Locate every P. falciparum parasite and identify its life-cycle stage.
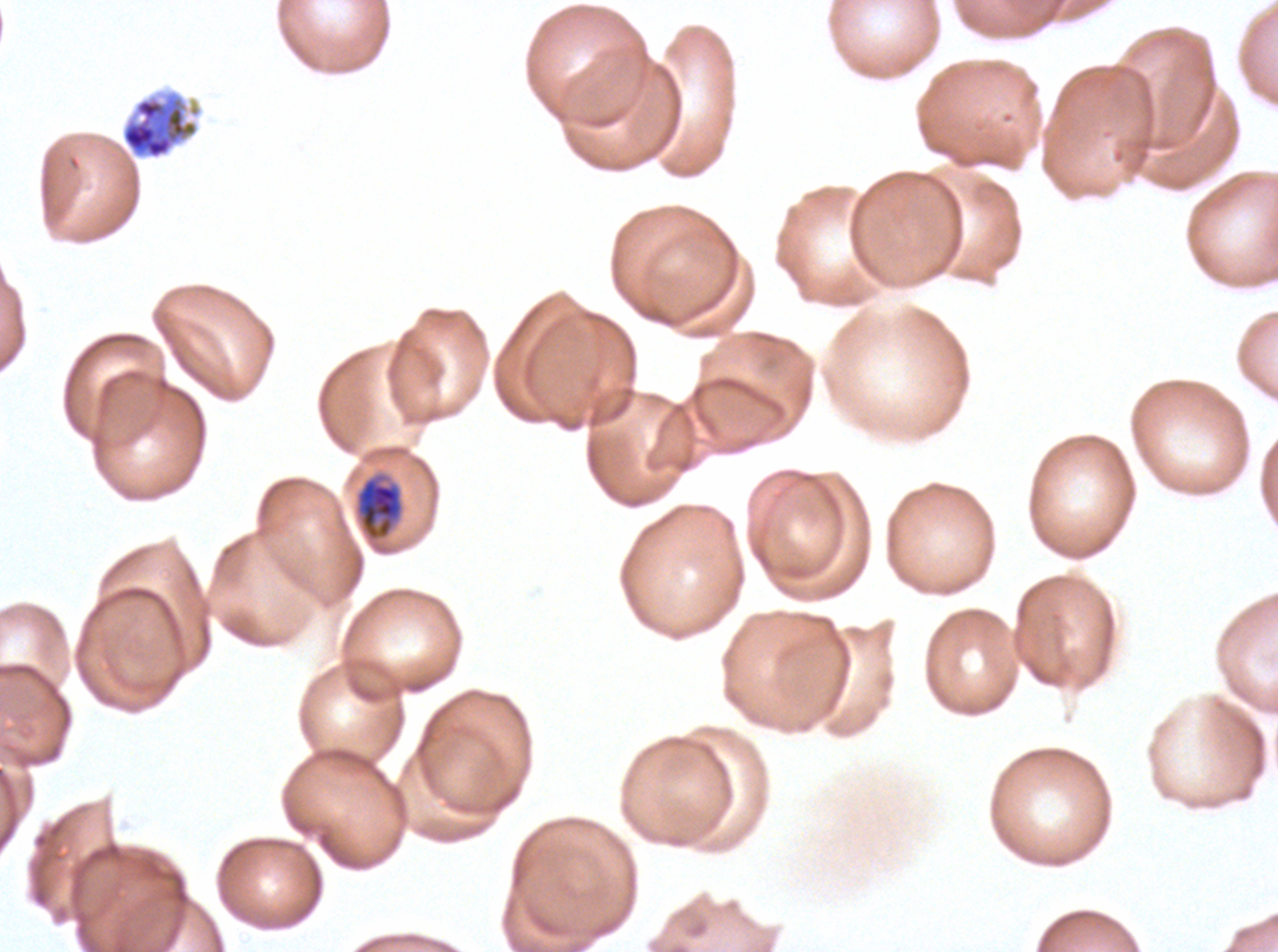

Approximate bounding boxes as (x1, y1, x2, y2) in pixels.
Late trophozoites: (355, 472, 404, 542).
Late schizonts: (120, 90, 203, 161).
No rings, late-ring/early-trophozoite forms, mid trophozoites, early schizonts, segmenters, or gametocytes observed.

preparation = thin blood smear
life-cycle stages observed = late trophozoite, late schizont
image size = 1278×952 pixels
field of view = sub-image separated from a larger composite
specimen = P. falciparum from a patient in The Gambia, cultured ex vivo for 24 to 48 hours
stain = Giemsa